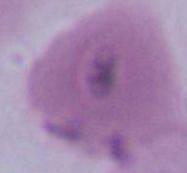
magnification = 1000x
modality = photomicrograph
identification = erythrocyte